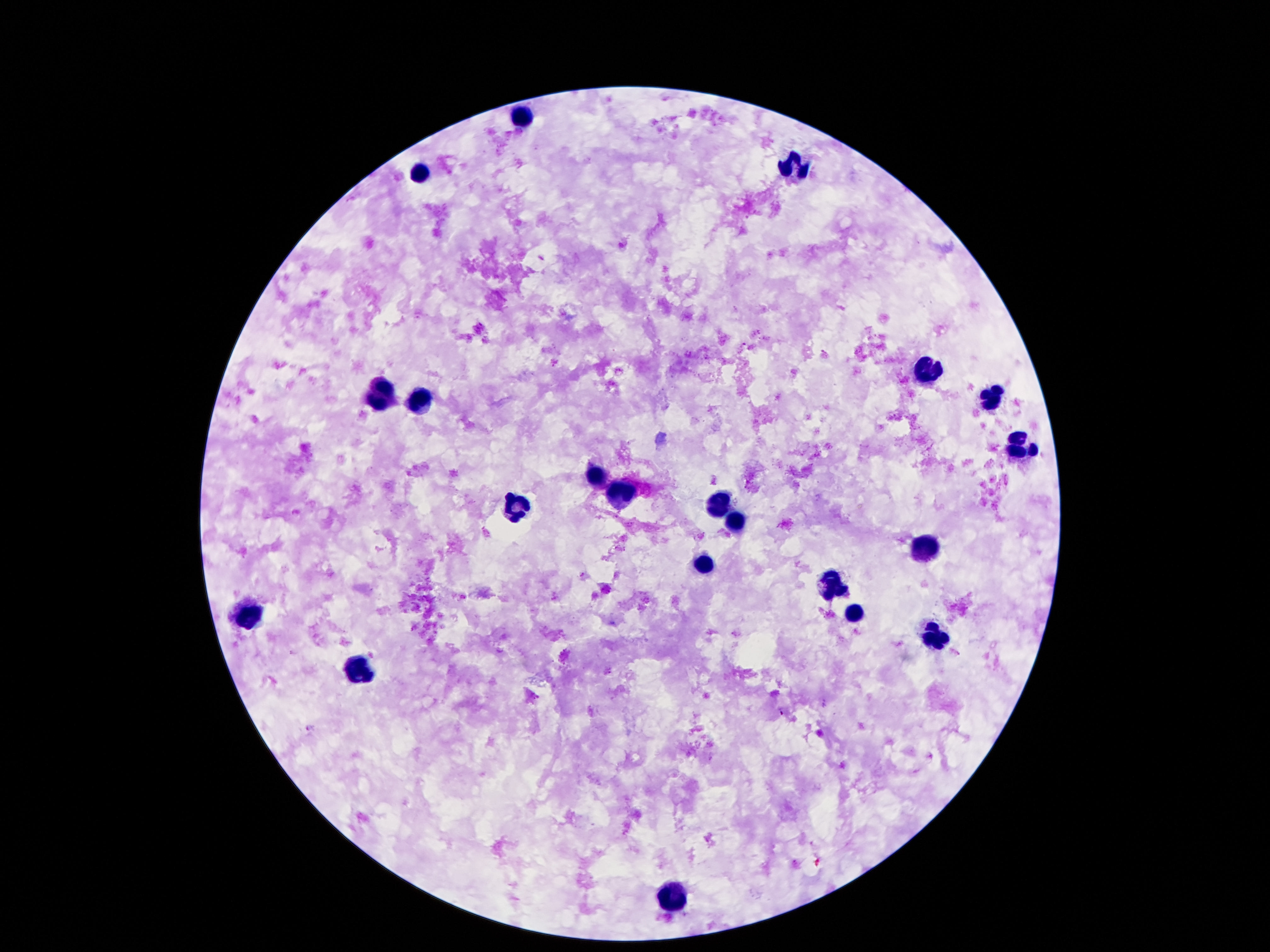 Approximate object centers, in pixels from the top-left corner. Leukocyte locations: (x=521, y=116), (x=794, y=169), (x=422, y=172), (x=928, y=371), (x=378, y=393), (x=422, y=397), (x=991, y=397), (x=1019, y=449), (x=594, y=478), (x=619, y=492), (x=515, y=508), (x=717, y=508), (x=730, y=523), (x=921, y=548), (x=703, y=569), (x=830, y=588), (x=855, y=613), (x=249, y=614), (x=937, y=638), (x=358, y=669), (x=676, y=898). Single field of view. Smartphone photograph taken through the microscope eyepiece. 100x magnification. Patient malaria status: negative. Image is 1270×952 pixels. Giemsa-stained preparation. Thick blood film.